Name the parasite shown.
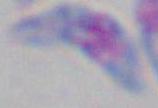
Toxoplasma gondii.

modality: micrograph
magnification: 1000x